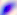
modality: photomicrograph
magnification: 400x
identification: Toxoplasma gondii